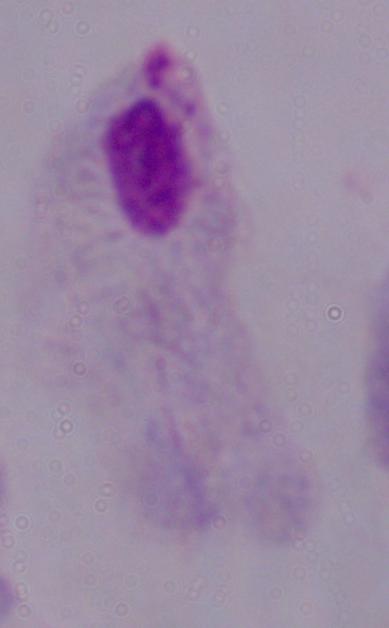
Summary:
  - Identification: trichomonad
  - Modality: micrograph
  - Magnification: 1000x